Identify the parasite.
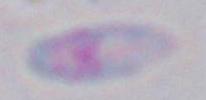

This is Toxoplasma gondii.

Micrograph. 1000x magnification.